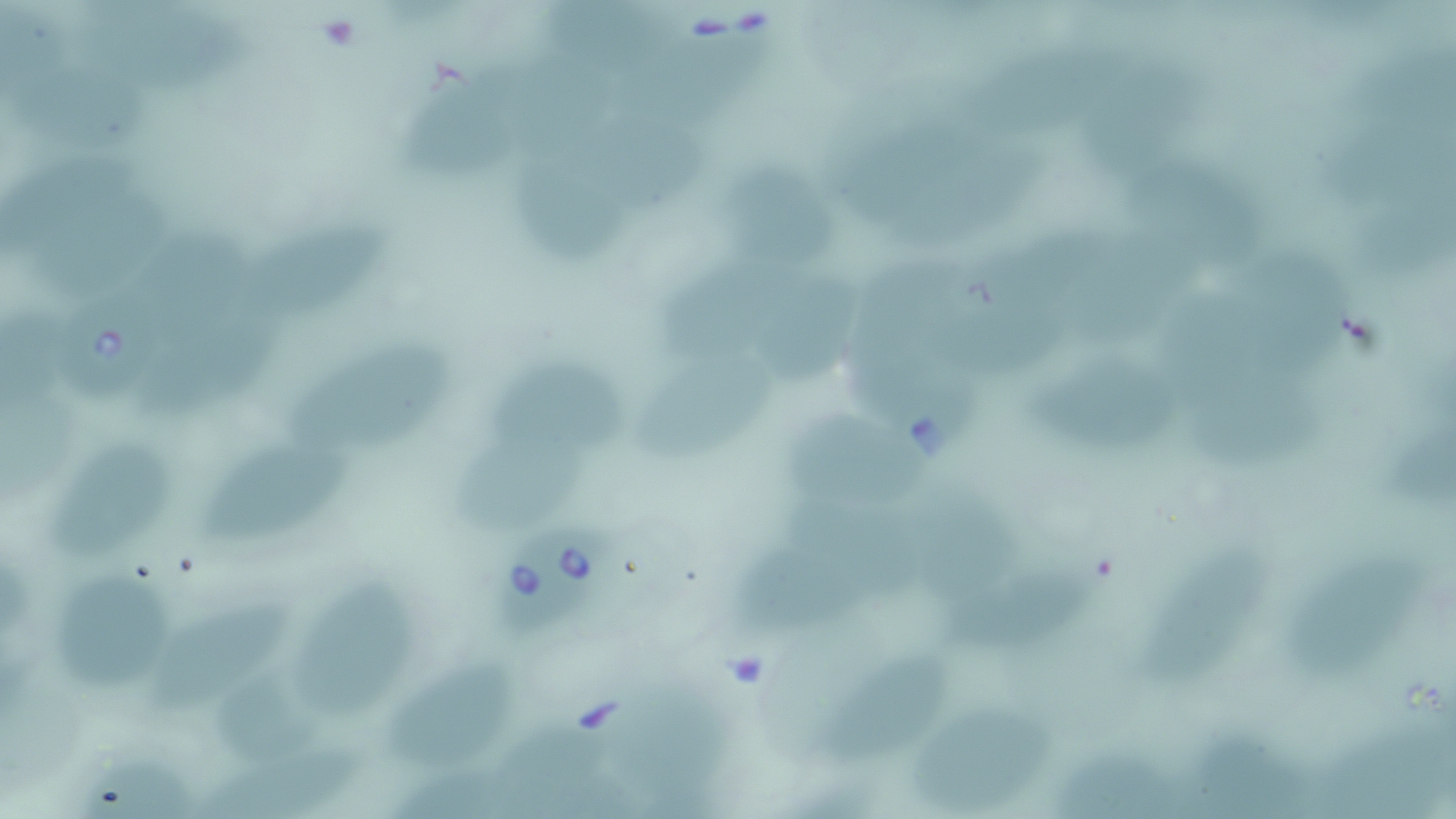
slide-level diagnosis = Babesia divergens
stain = May-Grünwald-Giemsa
preparation = thin blood smear
field of view = single
image size = 1456×819 pixels
magnification = 1000x
Babesia divergens-infected red blood cell locations = approximate bounding boxes as named x1/y1/x2/y2 corners in pixels: (x1=58, y1=297, x2=168, y2=401), (x1=501, y1=523, x2=617, y2=639)
modality = optical microscopy
uninfected red blood cell locations = approximate bounding boxes as named x1/y1/x2/y2 corners in pixels: (x1=550, y1=0, x2=674, y2=74), (x1=0, y1=5, x2=68, y2=97), (x1=72, y1=10, x2=269, y2=89), (x1=650, y1=27, x2=780, y2=125), (x1=972, y1=44, x2=1141, y2=128), (x1=1354, y1=50, x2=1453, y2=132), (x1=412, y1=66, x2=558, y2=175), (x1=1086, y1=73, x2=1201, y2=164), (x1=20, y1=81, x2=147, y2=147), (x1=576, y1=113, x2=708, y2=202), (x1=1334, y1=133, x2=1456, y2=216), (x1=12, y1=147, x2=146, y2=242), (x1=515, y1=148, x2=629, y2=265), (x1=1136, y1=161, x2=1272, y2=250), (x1=727, y1=166, x2=842, y2=251), (x1=35, y1=200, x2=178, y2=297), (x1=1349, y1=202, x2=1455, y2=278), (x1=249, y1=216, x2=381, y2=314), (x1=141, y1=231, x2=263, y2=312), (x1=1245, y1=249, x2=1349, y2=376), (x1=672, y1=253, x2=791, y2=364), (x1=846, y1=254, x2=971, y2=360), (x1=771, y1=265, x2=870, y2=377), (x1=1170, y1=289, x2=1271, y2=418), (x1=153, y1=300, x2=294, y2=412), (x1=3, y1=301, x2=71, y2=401), (x1=287, y1=326, x2=452, y2=448), (x1=634, y1=349, x2=771, y2=460), (x1=855, y1=353, x2=977, y2=460), (x1=1028, y1=353, x2=1184, y2=452), (x1=483, y1=364, x2=631, y2=440), (x1=1200, y1=371, x2=1339, y2=466), (x1=1, y1=391, x2=74, y2=501), (x1=800, y1=413, x2=928, y2=506), (x1=1389, y1=422, x2=1456, y2=511), (x1=444, y1=424, x2=593, y2=541), (x1=51, y1=442, x2=172, y2=565), (x1=200, y1=450, x2=343, y2=536), (x1=786, y1=495, x2=930, y2=596), (x1=917, y1=498, x2=1020, y2=605), (x1=749, y1=542, x2=871, y2=623), (x1=1134, y1=548, x2=1275, y2=702), (x1=1291, y1=550, x2=1402, y2=668), (x1=299, y1=565, x2=420, y2=708), (x1=56, y1=568, x2=177, y2=680), (x1=960, y1=570, x2=1093, y2=648), (x1=159, y1=584, x2=299, y2=698), (x1=393, y1=656, x2=519, y2=757), (x1=819, y1=656, x2=948, y2=767), (x1=208, y1=668, x2=316, y2=763), (x1=627, y1=683, x2=744, y2=790), (x1=910, y1=708, x2=1070, y2=805), (x1=501, y1=719, x2=610, y2=794), (x1=1317, y1=721, x2=1453, y2=819), (x1=1193, y1=734, x2=1306, y2=819), (x1=204, y1=741, x2=370, y2=819), (x1=1058, y1=749, x2=1195, y2=819), (x1=76, y1=751, x2=184, y2=817)